Classify this cell by malaria status.
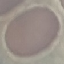
Uninfected.

image_type: automatically extracted cell patch, resized to 64 × 64 pixels
capture: smartphone camera at the microscope eyepiece
preparation: thin blood smear
stain: Giemsa